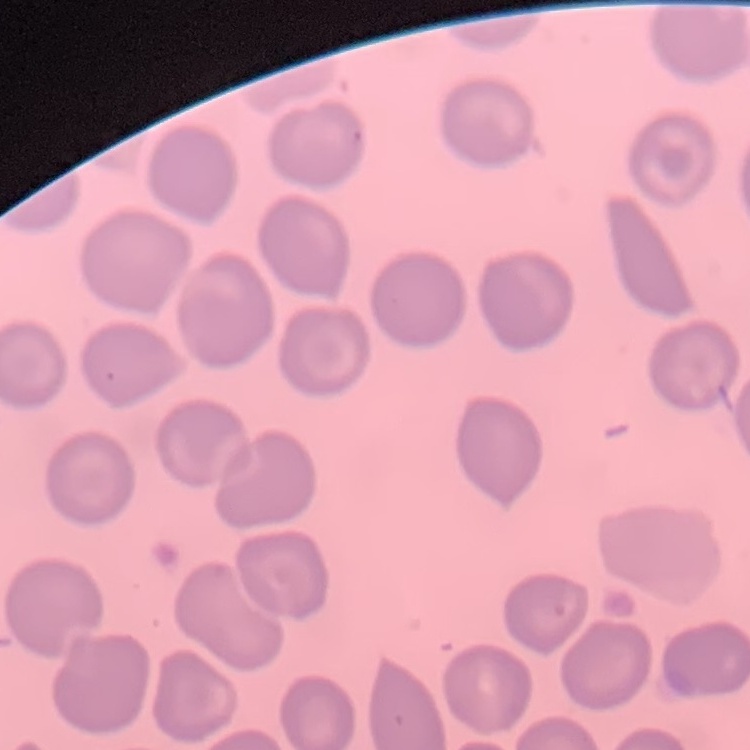

erythrocyte_morphology: no rouleaux formation
preparation: thin peripheral smear
stain: Field's or Giemsa
image_type: square crop of a larger photomicrograph